Give the extent of all Plasmodium falciparum-infected red blood cells.
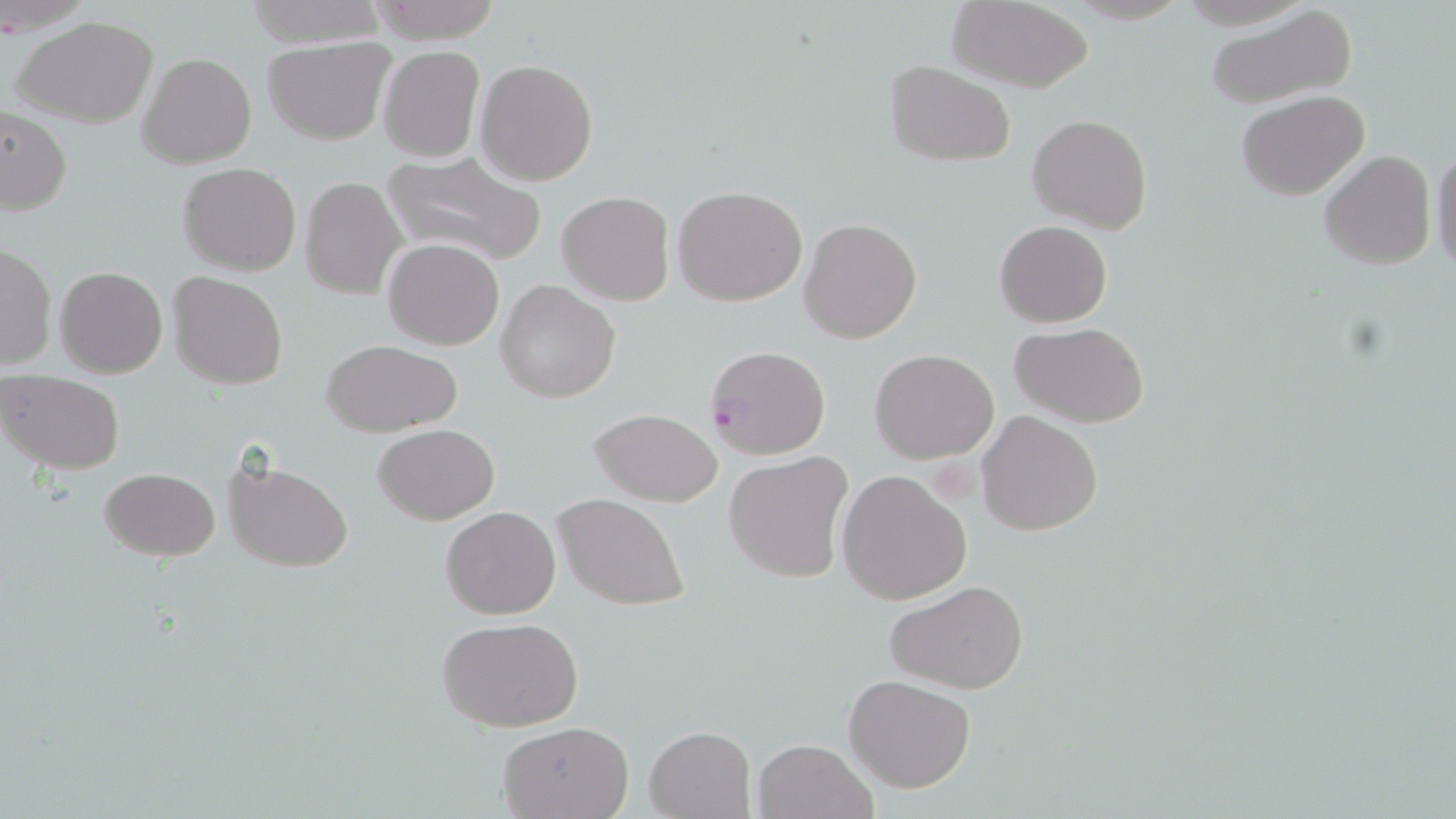

Approximate bounding boxes as named x1/y1/x2/y2 corners in pixels.
Plasmodium falciparum-infected red blood cells: (x1=707, y1=342, x2=831, y2=458).

Uninfected red blood cell locations: (x1=243, y1=0, x2=386, y2=47), (x1=364, y1=0, x2=501, y2=43), (x1=947, y1=1, x2=1096, y2=92), (x1=1204, y1=3, x2=1358, y2=111), (x1=15, y1=18, x2=157, y2=128), (x1=263, y1=37, x2=395, y2=146), (x1=377, y1=46, x2=484, y2=162), (x1=137, y1=53, x2=256, y2=171), (x1=476, y1=59, x2=599, y2=186), (x1=886, y1=61, x2=1016, y2=166), (x1=1236, y1=91, x2=1370, y2=201), (x1=1, y1=105, x2=72, y2=215), (x1=1027, y1=114, x2=1152, y2=234), (x1=1429, y1=141, x2=1455, y2=276), (x1=381, y1=150, x2=547, y2=268), (x1=1319, y1=150, x2=1436, y2=272), (x1=178, y1=163, x2=302, y2=276), (x1=306, y1=163, x2=489, y2=283), (x1=299, y1=176, x2=406, y2=300), (x1=673, y1=185, x2=807, y2=307), (x1=557, y1=191, x2=674, y2=307), (x1=799, y1=215, x2=923, y2=344), (x1=994, y1=219, x2=1113, y2=328), (x1=382, y1=238, x2=506, y2=351), (x1=0, y1=243, x2=55, y2=371), (x1=55, y1=266, x2=167, y2=378), (x1=169, y1=271, x2=287, y2=389), (x1=495, y1=279, x2=621, y2=403), (x1=1010, y1=322, x2=1151, y2=427), (x1=321, y1=338, x2=462, y2=438), (x1=869, y1=348, x2=999, y2=464), (x1=1, y1=370, x2=126, y2=474), (x1=589, y1=408, x2=724, y2=508), (x1=977, y1=410, x2=1104, y2=536), (x1=373, y1=424, x2=499, y2=526), (x1=724, y1=452, x2=854, y2=583), (x1=222, y1=458, x2=353, y2=572), (x1=99, y1=467, x2=219, y2=561), (x1=838, y1=470, x2=971, y2=605), (x1=553, y1=492, x2=690, y2=611), (x1=440, y1=504, x2=562, y2=620), (x1=887, y1=579, x2=1028, y2=695), (x1=436, y1=616, x2=586, y2=734), (x1=844, y1=674, x2=976, y2=793), (x1=495, y1=720, x2=635, y2=819), (x1=645, y1=726, x2=756, y2=819), (x1=752, y1=738, x2=877, y2=819). Slide-level diagnosis: Plasmodium falciparum. Image is 1456×819 pixels. 1000x magnification. Light microscopy. One field of a larger specimen. Thin blood film. May-Grünwald-Giemsa stain.